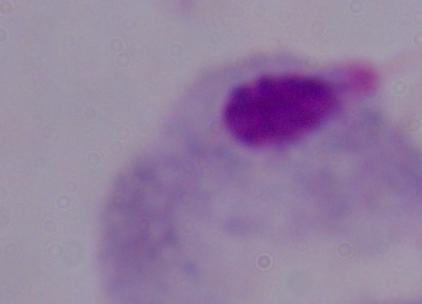
magnification = 1000x
modality = photomicrograph
identification = trichomonad